Describe the morphology of the erythrocytes.
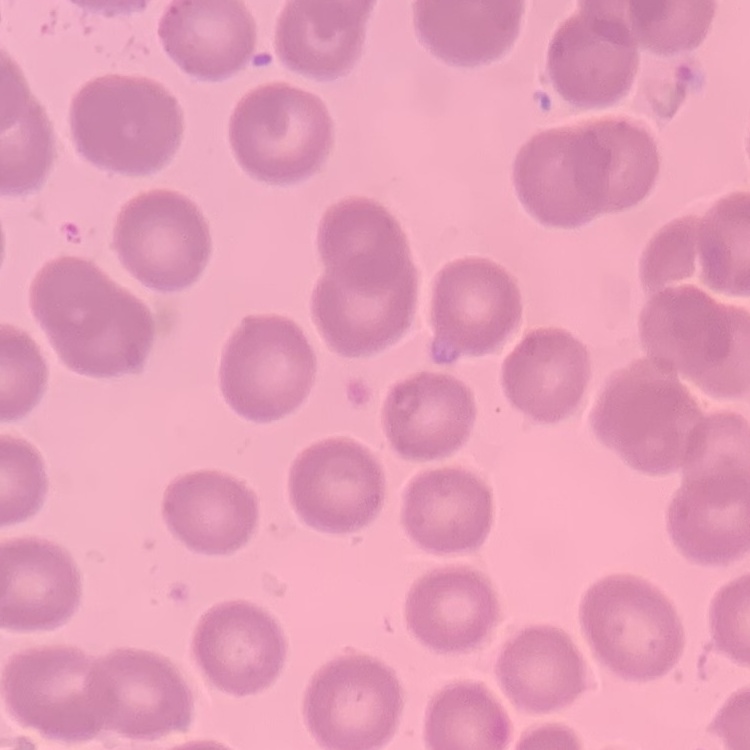
They show no rouleaux formation.

Summary:
  - Image type: one tile cut from a larger photomicrograph
  - Preparation: thin blood smear
  - Stain: Field's or Giemsa